Locate every malaria parasite by life-cycle stage, and every leukocyte.
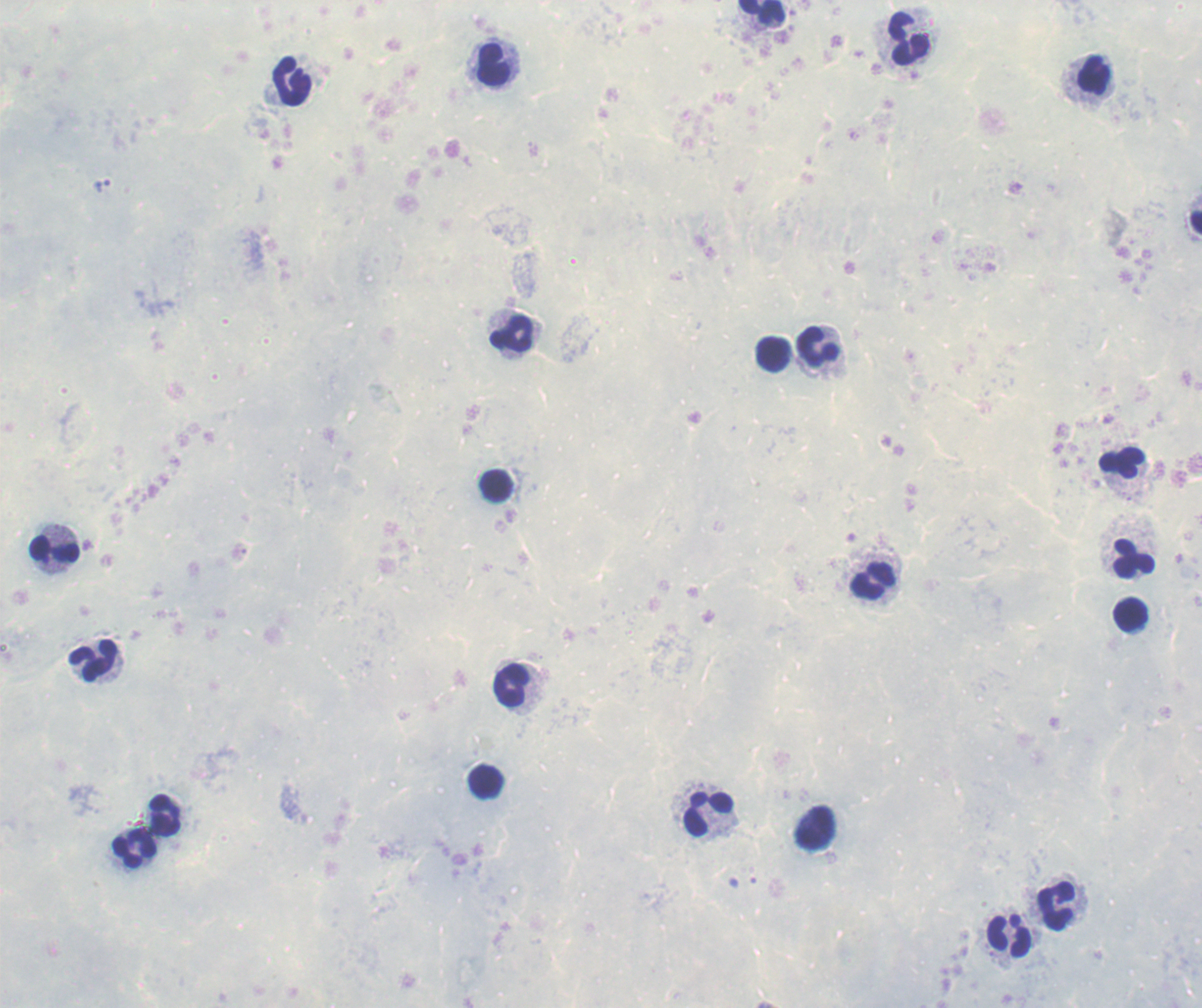

No malaria parasites detected.
Approximate object centers, in pixels from the top-left corner.
Leukocytes: (x=761, y=14), (x=908, y=39), (x=493, y=65), (x=1086, y=78), (x=293, y=81), (x=513, y=334), (x=819, y=348), (x=772, y=353), (x=1122, y=464), (x=495, y=486), (x=56, y=549), (x=1131, y=558), (x=873, y=580), (x=1130, y=616), (x=95, y=662), (x=516, y=684), (x=485, y=783), (x=707, y=813), (x=166, y=816), (x=816, y=828), (x=135, y=848), (x=1056, y=906), (x=1010, y=935).

Summary:
  - Image size: 1202×1008 pixels
  - Magnification: 100x
  - Background quality: poor
  - Context: previously used in a real diagnosis
  - Stain: Romanowsky
  - Field of view: one from this slide
  - Preparation: thick blood smear